State which parasite is depicted.
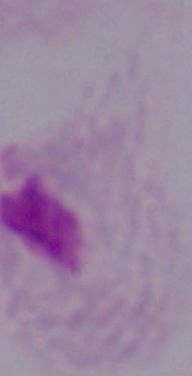

A trichomonad.

1000x magnification. Micrograph.